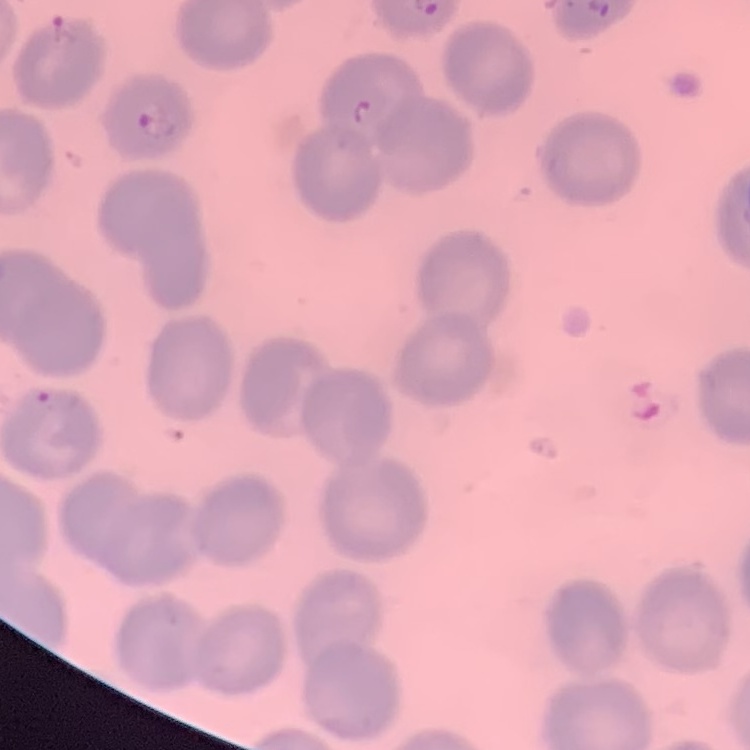

red blood cell morphology = no rouleaux formation
preparation = thin blood film
stain = Field's or Giemsa
image type = one tile cut from a larger photomicrograph